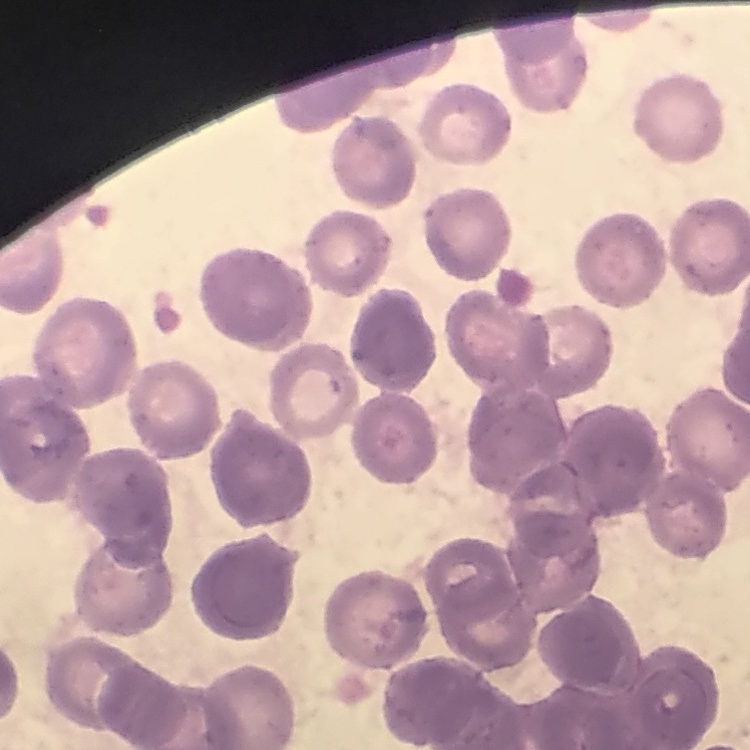

erythrocyte morphology = rouleaux formation
image type = one tile cut from a larger photomicrograph
preparation = thin blood film
stain = Field's or Giemsa